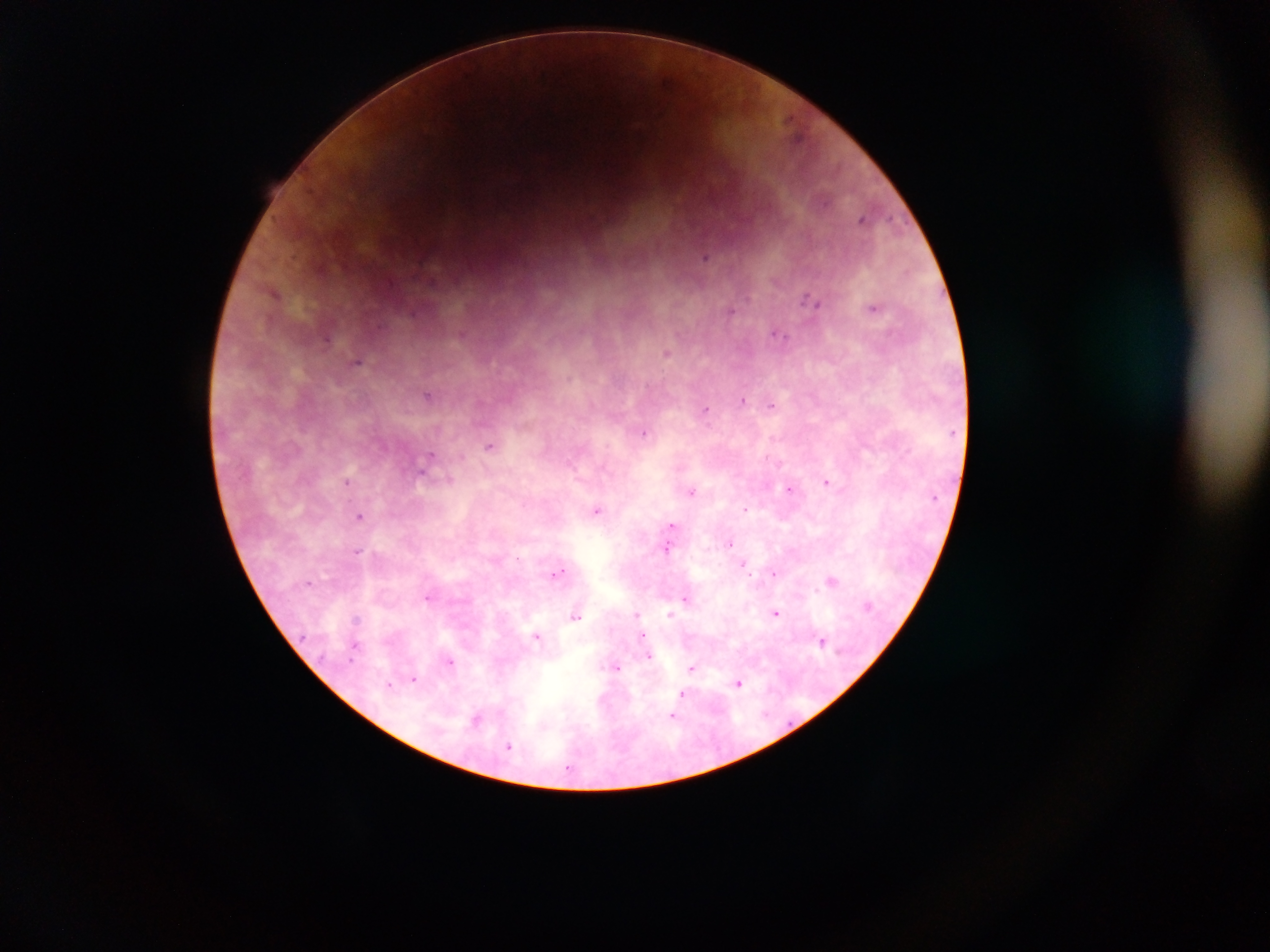

Approximate centers as {x, y} in pixels.
Summary:
  - Malaria parasite locations: {666, 80}, {797, 135}, {862, 219}, {706, 257}, {276, 293}, {811, 300}, {873, 307}, {413, 312}, {730, 312}, {777, 333}, {327, 338}, {666, 352}, {357, 362}, {427, 395}, {743, 400}, {772, 405}, {706, 411}, {643, 432}, {489, 446}, {430, 459}, {425, 469}, {347, 481}, {450, 481}, {827, 482}, {789, 489}, {692, 491}, {745, 509}, {596, 510}, {359, 516}, {671, 525}, {730, 544}, {667, 549}, {357, 551}, {743, 564}, {558, 572}, {774, 573}, {831, 581}, {428, 598}, {686, 599}, {637, 614}, {775, 614}, {671, 615}, {576, 616}, {356, 619}, {537, 637}, {822, 641}, {356, 644}, {645, 646}, {649, 657}, {450, 662}, {614, 668}, {692, 668}, {414, 678}, {739, 683}, {390, 684}, {682, 696}, {678, 706}, {674, 715}, {477, 719}, {509, 747}
  - Capture: mobile-phone photograph through a microscope
  - Preparation: thick blood film
  - Field of view: single
  - Image size: 1270×952 pixels
  - Country: Ghana